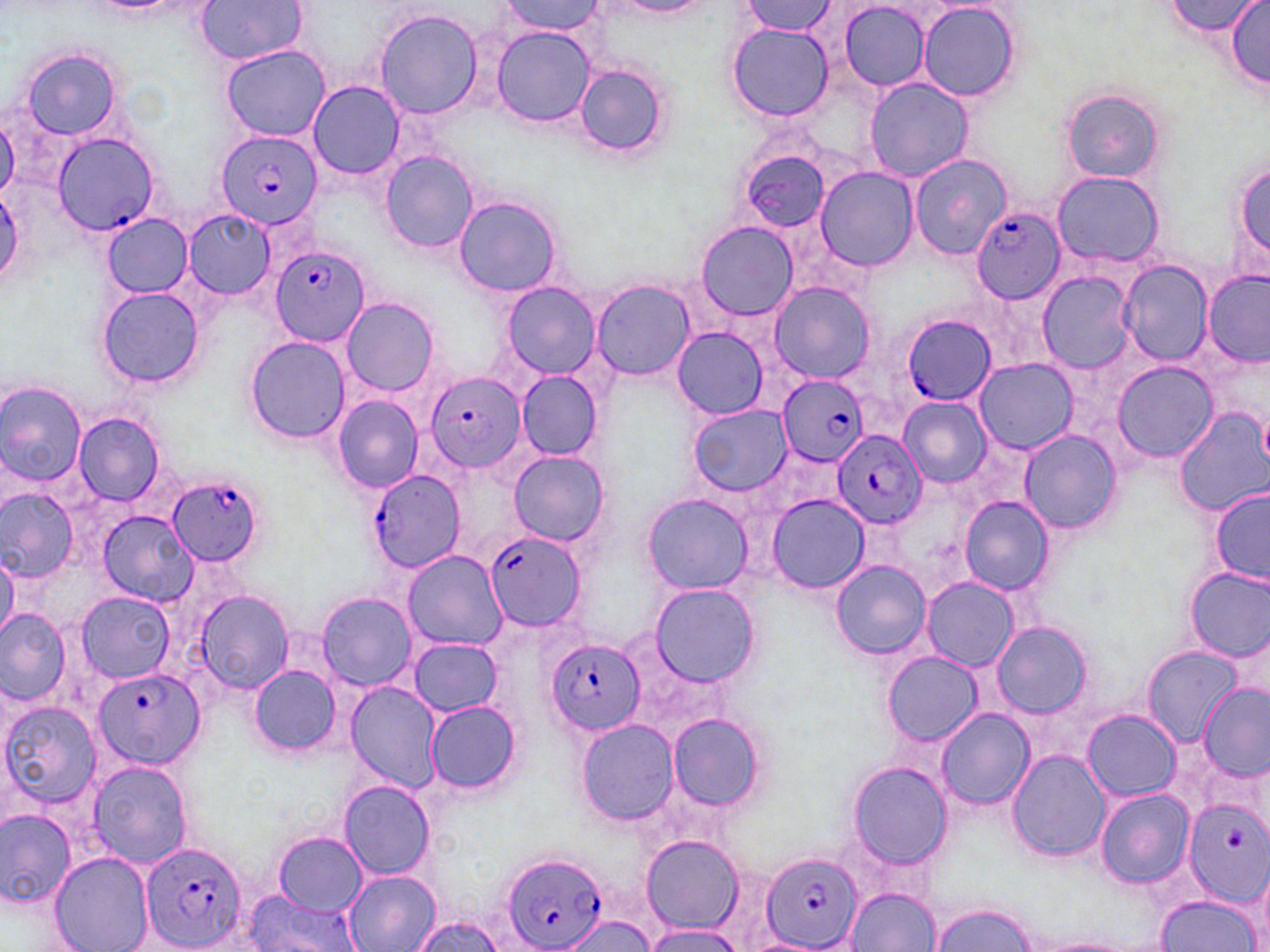
slide-level diagnosis = Plasmodium falciparum
modality = optical microscopy
Plasmodium falciparum-infected red blood cell locations = approximate bounding boxes as named x1/y1/x2/y2 corners in pixels: (x1=215, y1=129, x2=322, y2=231), (x1=52, y1=132, x2=160, y2=236), (x1=971, y1=204, x2=1067, y2=303), (x1=272, y1=245, x2=370, y2=346), (x1=900, y1=313, x2=997, y2=406), (x1=424, y1=370, x2=526, y2=474), (x1=777, y1=375, x2=871, y2=465), (x1=832, y1=430, x2=926, y2=529), (x1=365, y1=468, x2=467, y2=575), (x1=167, y1=474, x2=263, y2=567), (x1=484, y1=529, x2=586, y2=633), (x1=547, y1=638, x2=644, y2=736), (x1=91, y1=665, x2=205, y2=773), (x1=1182, y1=798, x2=1270, y2=906), (x1=141, y1=841, x2=249, y2=952), (x1=764, y1=849, x2=863, y2=952), (x1=500, y1=850, x2=608, y2=952)
magnification = 1000x
image size = 1270×952 pixels
preparation = thin blood film
uninfected red blood cell locations = approximate bounding boxes as named x1/y1/x2/y2 corners in pixels: (x1=192, y1=0, x2=310, y2=62), (x1=740, y1=0, x2=835, y2=37), (x1=499, y1=1, x2=605, y2=36), (x1=616, y1=1, x2=707, y2=17), (x1=839, y1=1, x2=932, y2=92), (x1=1166, y1=1, x2=1260, y2=39), (x1=1225, y1=1, x2=1270, y2=87), (x1=917, y1=2, x2=1020, y2=101), (x1=198, y1=9, x2=318, y2=112), (x1=374, y1=9, x2=484, y2=120), (x1=725, y1=22, x2=836, y2=122), (x1=489, y1=25, x2=595, y2=126), (x1=220, y1=45, x2=329, y2=141), (x1=20, y1=48, x2=124, y2=140), (x1=572, y1=61, x2=671, y2=160), (x1=864, y1=77, x2=973, y2=183), (x1=306, y1=80, x2=407, y2=180), (x1=1060, y1=90, x2=1165, y2=183), (x1=1, y1=111, x2=19, y2=200), (x1=378, y1=150, x2=479, y2=253), (x1=908, y1=153, x2=1013, y2=259), (x1=1231, y1=156, x2=1270, y2=269), (x1=814, y1=167, x2=918, y2=270), (x1=1050, y1=170, x2=1165, y2=266), (x1=452, y1=197, x2=564, y2=297), (x1=181, y1=208, x2=277, y2=299), (x1=102, y1=215, x2=193, y2=296), (x1=695, y1=221, x2=799, y2=322), (x1=1118, y1=259, x2=1211, y2=365), (x1=1202, y1=270, x2=1269, y2=366), (x1=1039, y1=271, x2=1136, y2=373), (x1=591, y1=280, x2=697, y2=380), (x1=767, y1=281, x2=875, y2=383), (x1=501, y1=282, x2=602, y2=379), (x1=97, y1=285, x2=204, y2=390), (x1=341, y1=297, x2=439, y2=396), (x1=671, y1=327, x2=769, y2=418), (x1=243, y1=336, x2=351, y2=444), (x1=976, y1=358, x2=1076, y2=453), (x1=1110, y1=362, x2=1218, y2=463), (x1=515, y1=371, x2=603, y2=461), (x1=0, y1=381, x2=87, y2=489), (x1=332, y1=395, x2=423, y2=492), (x1=899, y1=398, x2=990, y2=485), (x1=688, y1=406, x2=794, y2=497), (x1=1176, y1=408, x2=1270, y2=514), (x1=72, y1=411, x2=165, y2=507), (x1=1018, y1=429, x2=1120, y2=535), (x1=507, y1=450, x2=610, y2=547), (x1=0, y1=486, x2=79, y2=584), (x1=1210, y1=490, x2=1269, y2=583), (x1=641, y1=492, x2=754, y2=596), (x1=766, y1=493, x2=868, y2=595), (x1=960, y1=497, x2=1055, y2=596), (x1=99, y1=511, x2=199, y2=608), (x1=0, y1=550, x2=18, y2=642), (x1=402, y1=551, x2=507, y2=650), (x1=830, y1=560, x2=931, y2=660), (x1=1185, y1=566, x2=1270, y2=662), (x1=922, y1=578, x2=1019, y2=671), (x1=649, y1=584, x2=761, y2=688), (x1=193, y1=590, x2=292, y2=695), (x1=76, y1=592, x2=176, y2=682), (x1=315, y1=592, x2=419, y2=691), (x1=0, y1=609, x2=71, y2=706), (x1=991, y1=620, x2=1094, y2=720), (x1=409, y1=638, x2=501, y2=716), (x1=1142, y1=647, x2=1244, y2=744), (x1=881, y1=652, x2=983, y2=746), (x1=249, y1=665, x2=342, y2=754), (x1=345, y1=682, x2=443, y2=791), (x1=1197, y1=684, x2=1270, y2=781), (x1=2, y1=700, x2=102, y2=809), (x1=425, y1=700, x2=522, y2=794), (x1=935, y1=708, x2=1035, y2=809), (x1=1082, y1=710, x2=1181, y2=801), (x1=668, y1=714, x2=765, y2=814), (x1=577, y1=720, x2=678, y2=825), (x1=1005, y1=747, x2=1111, y2=864), (x1=87, y1=760, x2=193, y2=870), (x1=848, y1=761, x2=952, y2=871), (x1=339, y1=779, x2=437, y2=880), (x1=1094, y1=787, x2=1196, y2=888), (x1=1, y1=807, x2=75, y2=910), (x1=273, y1=832, x2=366, y2=915), (x1=642, y1=835, x2=743, y2=932), (x1=48, y1=850, x2=154, y2=951), (x1=1255, y1=862, x2=1270, y2=950), (x1=344, y1=871, x2=440, y2=952), (x1=849, y1=887, x2=941, y2=951), (x1=240, y1=890, x2=363, y2=952), (x1=1156, y1=894, x2=1260, y2=950), (x1=929, y1=904, x2=1036, y2=952), (x1=557, y1=914, x2=655, y2=952), (x1=411, y1=915, x2=505, y2=952), (x1=640, y1=923, x2=744, y2=952), (x1=1030, y1=937, x2=1140, y2=952)
field of view = single
stain = May-Grünwald-Giemsa